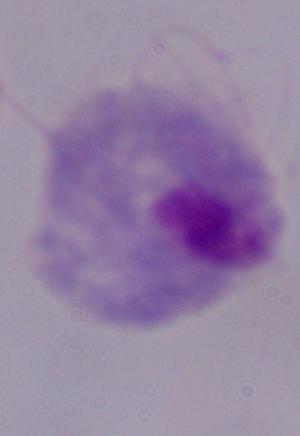 A trichomonad is shown. 1000x magnification. Photomicrograph.